Classify this cell by malaria status.
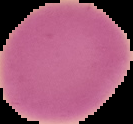
It is uninfected.

Summary:
  - Preparation: thin blood smear
  - Image type: segmented cell region with the area outside set to black
  - Image size: 133×124 pixels